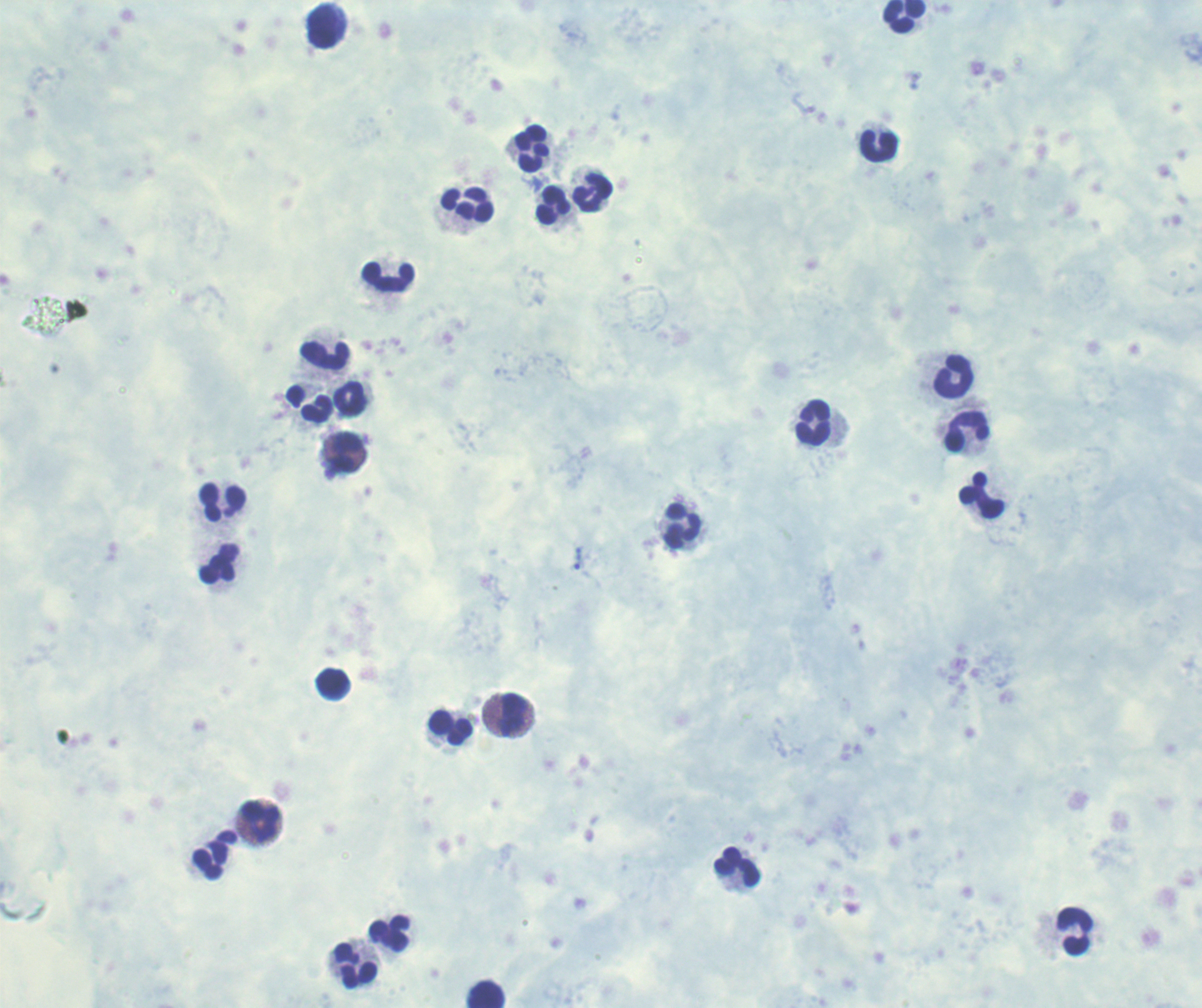 Approximate object centers, in pixels from the top-left corner. Leukocyte locations: (x=904, y=16), (x=324, y=27), (x=879, y=147), (x=532, y=149), (x=593, y=193), (x=468, y=205), (x=554, y=206), (x=388, y=277), (x=325, y=357), (x=954, y=377), (x=349, y=400), (x=317, y=410), (x=814, y=424), (x=967, y=432), (x=345, y=453), (x=982, y=496), (x=224, y=502), (x=683, y=527), (x=220, y=565), (x=333, y=685), (x=514, y=715), (x=451, y=729), (x=261, y=823), (x=211, y=862), (x=738, y=868), (x=1075, y=931), (x=390, y=934), (x=356, y=967), (x=487, y=995). Trophozoite locations: (x=578, y=559). Thick blood smear. Background quality: poor. Previously used in a real diagnosis. Captured at 100x magnification. Single field of view. Result: Plasmodium parasites identified. Image is 1202×1008 pixels. Romanowsky stain.